Give the extent of all Plasmodium falciparum-infected red blood cells.
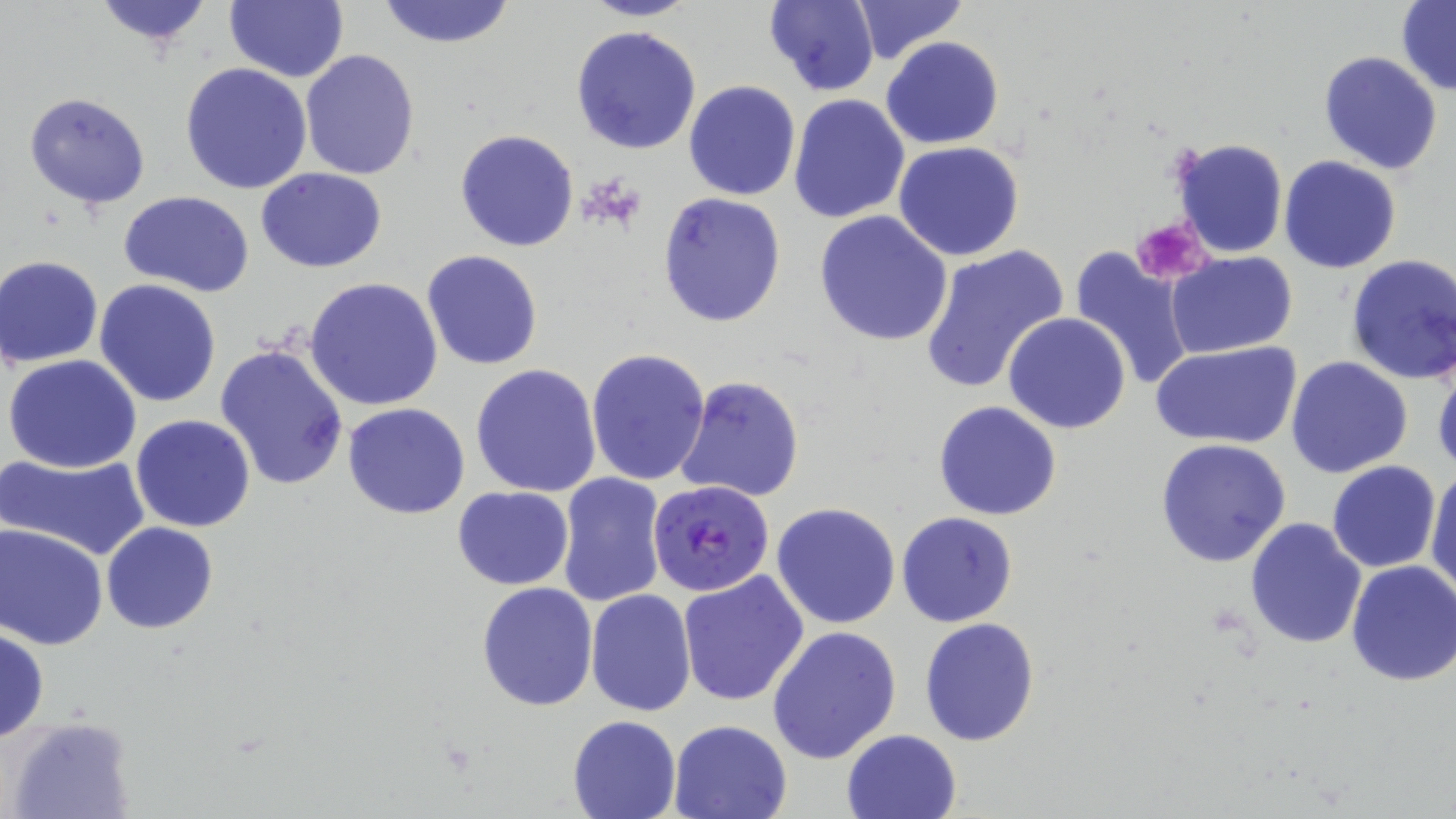

Approximate bounding boxes as (x1, y1, x2, y2) in pixels.
Plasmodium falciparum-infected red blood cells: (649, 480, 774, 597).

slide_level_diagnosis: Plasmodium falciparum
uninfected_red_blood_cell_locations: 'approximate bounding boxes as (x1, y1, x2, y2) in pixels: (89, 0, 219, 51), (224, 0, 347, 82), (374, 0, 519, 50), (580, 0, 702, 22), (853, 0, 967, 62), (1397, 0, 1456, 95), (763, 1, 881, 95), (571, 24, 702, 156), (881, 37, 1003, 150), (300, 49, 420, 180), (808, 49, 953, 186), (1317, 50, 1443, 176), (179, 63, 313, 195), (682, 80, 802, 201), (24, 93, 150, 209), (788, 94, 911, 224), (455, 129, 580, 251), (1171, 137, 1288, 258), (893, 140, 1025, 260), (1279, 155, 1403, 274), (255, 167, 387, 273), (121, 191, 256, 296), (657, 192, 786, 327), (814, 211, 953, 346), (918, 244, 1068, 395), (1067, 244, 1197, 393), (421, 249, 544, 370), (1166, 251, 1297, 358), (1344, 252, 1456, 386), (1, 255, 104, 366), (304, 277, 443, 413), (94, 279, 221, 407), (1002, 311, 1132, 434), (1152, 341, 1299, 451), (214, 345, 350, 491), (586, 349, 711, 487), (1431, 350, 1456, 479), (4, 354, 145, 474), (1285, 356, 1414, 478), (470, 364, 602, 499), (676, 377, 807, 501), (933, 400, 1062, 520), (343, 403, 470, 518), (130, 413, 257, 532), (1153, 439, 1293, 568), (1, 451, 152, 561), (1326, 459, 1442, 572), (1426, 465, 1456, 599), (556, 473, 669, 609), (452, 485, 574, 591), (771, 502, 902, 630), (896, 512, 1018, 627), (1243, 517, 1367, 650), (101, 522, 218, 634), (1, 523, 107, 650), (1344, 561, 1456, 686), (677, 570, 808, 707), (477, 582, 599, 710), (586, 589, 697, 717), (919, 616, 1040, 745), (0, 626, 49, 743), (767, 626, 901, 765), (567, 714, 682, 818), (4, 715, 137, 819), (668, 719, 793, 819), (841, 729, 963, 819)'
magnification: 1000x
image_size: 1456×819 pixels
field_of_view: single
modality: light microscopy
stain: May-Grünwald-Giemsa
platelet_locations: 'approximate bounding boxes as (x1, y1, x2, y2) in pixels: (1130, 217, 1211, 285)'
preparation: thin blood smear